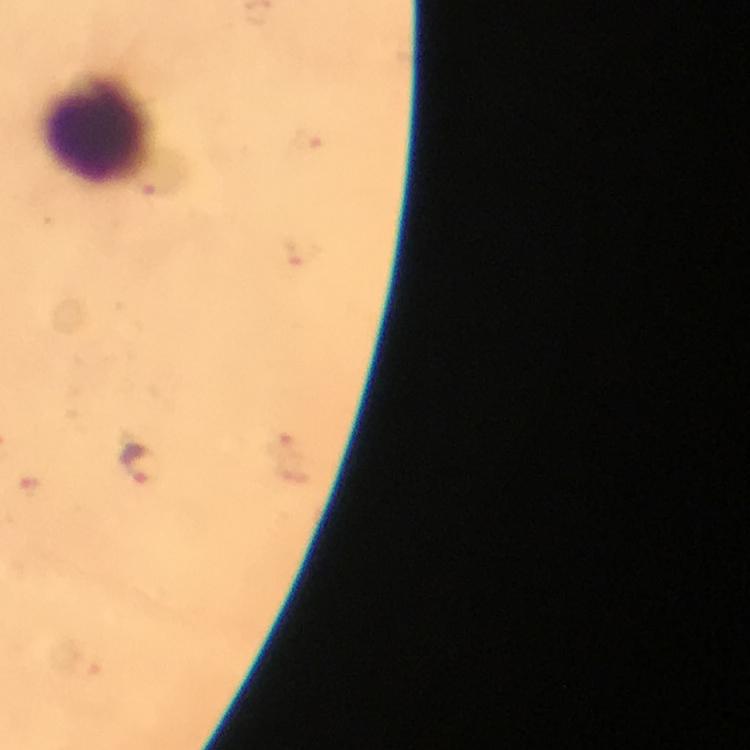
Approximate object centers, in pixels from the top-left corner. Leukocyte locations: (x=97, y=131). Malaria parasite locations: (x=308, y=140), (x=141, y=466). Smartphone photograph taken through a microscope. From a malaria diagnostic workup. Image is 750×750 pixels. Immersion oil applied. 100x magnification. Thick blood smear. A crop from one field of view. Giemsa stain.